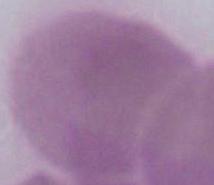

Photomicrograph. Captured at 1000x magnification. An erythrocyte is shown.